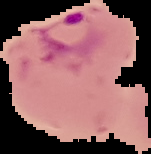

Segmented cell region on a black background. From a thin blood film. Malaria status: parasitized. Image is 151×154 pixels.